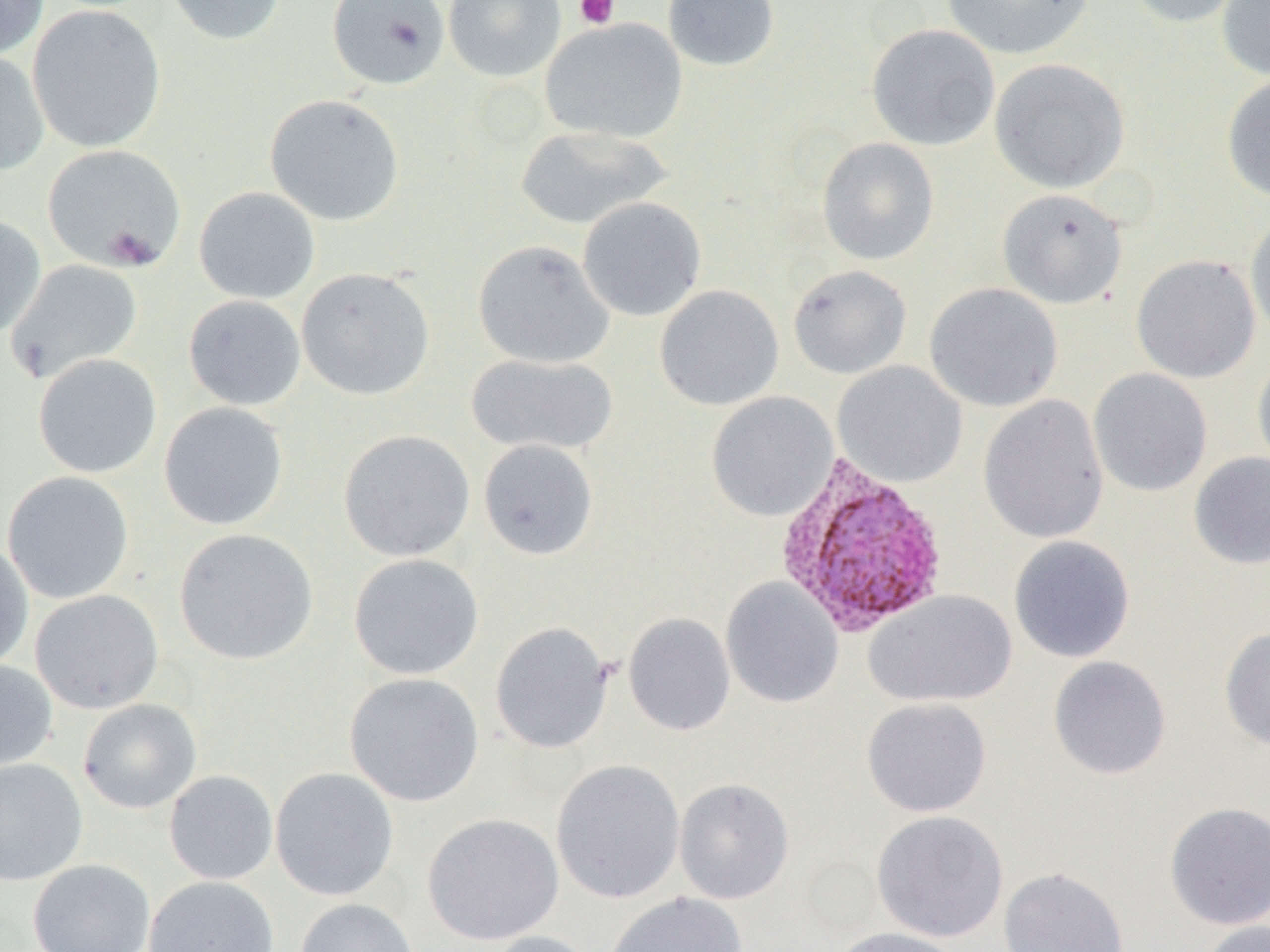
{
  "plasmodium_vivax_infected_red_blood_cell_locations": "approximate bounding boxes as named x1/y1/x2/y2 corners in pixels: (x1=774, y1=455, x2=951, y2=637)",
  "slide_level_diagnosis": "Plasmodium vivax",
  "preparation": "thin blood film",
  "modality": "optical microscopy",
  "magnification": "1000x",
  "uninfected_red_blood_cell_locations": "approximate bounding boxes as named x1/y1/x2/y2 corners in pixels: (x1=0, y1=0, x2=49, y2=60), (x1=163, y1=0, x2=285, y2=45), (x1=327, y1=0, x2=450, y2=90), (x1=443, y1=0, x2=566, y2=82), (x1=662, y1=0, x2=780, y2=71), (x1=940, y1=0, x2=1095, y2=60), (x1=1124, y1=0, x2=1249, y2=28), (x1=1216, y1=0, x2=1270, y2=81), (x1=27, y1=4, x2=166, y2=152), (x1=540, y1=17, x2=687, y2=144), (x1=866, y1=23, x2=1000, y2=151), (x1=0, y1=50, x2=50, y2=176), (x1=989, y1=58, x2=1130, y2=193), (x1=1221, y1=74, x2=1270, y2=203), (x1=264, y1=93, x2=405, y2=226), (x1=514, y1=124, x2=672, y2=231), (x1=816, y1=137, x2=939, y2=265), (x1=42, y1=144, x2=186, y2=272), (x1=194, y1=187, x2=320, y2=304), (x1=997, y1=188, x2=1128, y2=310), (x1=577, y1=197, x2=707, y2=322), (x1=1245, y1=208, x2=1270, y2=343), (x1=0, y1=215, x2=46, y2=339), (x1=473, y1=239, x2=614, y2=369), (x1=1130, y1=254, x2=1260, y2=383), (x1=5, y1=259, x2=143, y2=384), (x1=788, y1=265, x2=911, y2=379), (x1=296, y1=267, x2=435, y2=400), (x1=924, y1=282, x2=1063, y2=412), (x1=654, y1=285, x2=784, y2=411), (x1=183, y1=295, x2=305, y2=411), (x1=32, y1=353, x2=162, y2=478), (x1=466, y1=353, x2=618, y2=456), (x1=1252, y1=353, x2=1270, y2=479), (x1=832, y1=361, x2=967, y2=488), (x1=1088, y1=368, x2=1213, y2=497), (x1=706, y1=392, x2=838, y2=522), (x1=977, y1=394, x2=1109, y2=544), (x1=158, y1=402, x2=289, y2=531), (x1=338, y1=429, x2=475, y2=562), (x1=477, y1=439, x2=599, y2=561), (x1=1189, y1=452, x2=1270, y2=570), (x1=2, y1=471, x2=134, y2=604), (x1=174, y1=528, x2=318, y2=665), (x1=1009, y1=535, x2=1135, y2=663), (x1=0, y1=541, x2=34, y2=673), (x1=348, y1=553, x2=484, y2=680), (x1=720, y1=577, x2=844, y2=709), (x1=30, y1=589, x2=163, y2=714), (x1=863, y1=589, x2=1017, y2=708), (x1=623, y1=613, x2=736, y2=736), (x1=490, y1=621, x2=614, y2=753), (x1=1219, y1=626, x2=1270, y2=750), (x1=1047, y1=655, x2=1172, y2=780), (x1=0, y1=660, x2=57, y2=773), (x1=344, y1=672, x2=484, y2=807), (x1=861, y1=697, x2=992, y2=817), (x1=78, y1=698, x2=201, y2=814), (x1=0, y1=757, x2=88, y2=886), (x1=551, y1=759, x2=685, y2=904), (x1=270, y1=767, x2=399, y2=901), (x1=164, y1=770, x2=278, y2=884), (x1=674, y1=778, x2=794, y2=904), (x1=1163, y1=802, x2=1270, y2=930), (x1=871, y1=810, x2=1009, y2=942), (x1=422, y1=813, x2=564, y2=946), (x1=27, y1=859, x2=155, y2=952), (x1=998, y1=866, x2=1130, y2=952), (x1=143, y1=876, x2=280, y2=952), (x1=603, y1=891, x2=748, y2=952), (x1=294, y1=898, x2=419, y2=952), (x1=1197, y1=919, x2=1270, y2=952), (x1=830, y1=927, x2=966, y2=952), (x1=481, y1=930, x2=603, y2=952)",
  "field_of_view": "single",
  "image_size": "1270×952 pixels",
  "platelet_locations": "approximate bounding boxes as named x1/y1/x2/y2 corners in pixels: (x1=573, y1=0, x2=620, y2=29)"
}